Assess this cell for malaria.
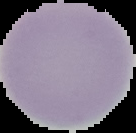

It is uninfected.

preparation = thin blood smear
image type = segmented cell region with the area outside set to black
image size = 136×133 pixels